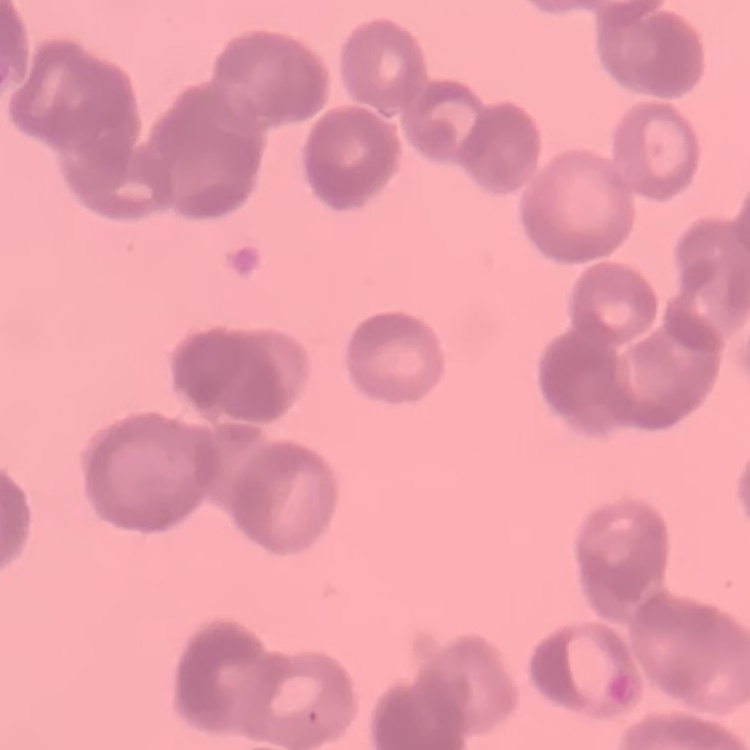 The red blood cells show rouleaux formation. Stained with either Field's or Giemsa. Square crop of a larger photomicrograph. Thin peripheral smear.